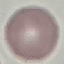
Summary:
  - Result: no malaria parasites seen
  - Capture: smartphone through the microscope eyepiece
  - Preparation: thin blood film
  - Image type: cell patch, automatically extracted from a larger field of view and resized to 64 × 64 pixels
  - Stain: Giemsa